Outline each blood parasite and name the species.
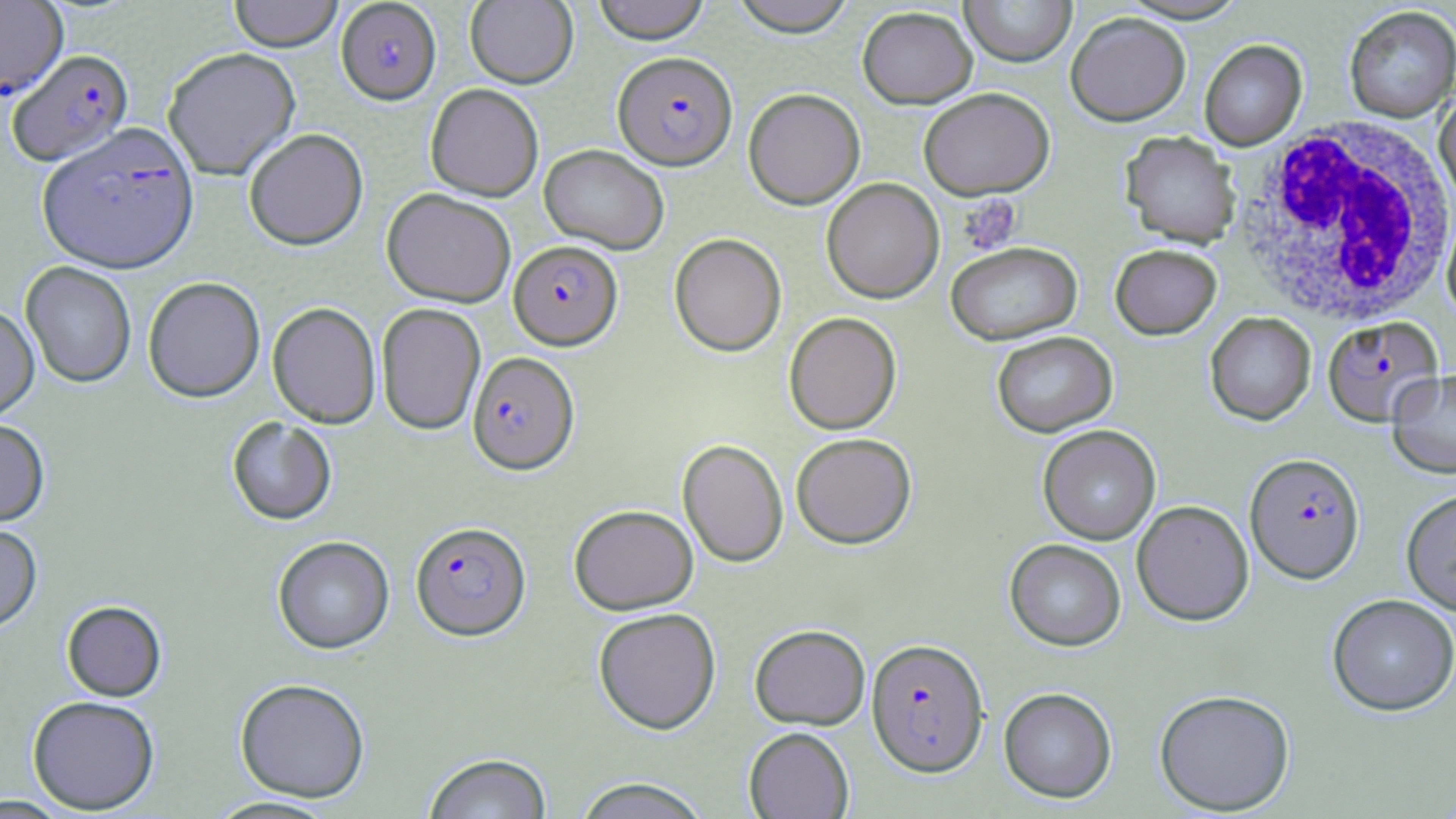

Approximate bounding boxes as named x1/y1/x2/y2 corners in pixels.
Plasmodium falciparum-infected red blood cells: (x1=0, y1=0, x2=67, y2=102), (x1=335, y1=1, x2=442, y2=106), (x1=7, y1=50, x2=134, y2=168), (x1=614, y1=51, x2=737, y2=169), (x1=37, y1=128, x2=199, y2=277), (x1=508, y1=241, x2=622, y2=350), (x1=1322, y1=315, x2=1443, y2=425), (x1=467, y1=352, x2=579, y2=476), (x1=1245, y1=452, x2=1364, y2=583), (x1=410, y1=521, x2=531, y2=642), (x1=866, y1=638, x2=988, y2=777).
No Plasmodium ovale, Plasmodium malariae, Plasmodium vivax, Babesia divergens, or Trypanosoma brucei observed.

Platelet locations: (x1=958, y1=194, x2=1022, y2=255). White blood cell locations: (x1=1233, y1=117, x2=1455, y2=326). Uninfected red blood cell locations: (x1=228, y1=0, x2=343, y2=54), (x1=465, y1=0, x2=578, y2=88), (x1=592, y1=0, x2=711, y2=43), (x1=729, y1=0, x2=857, y2=36), (x1=959, y1=0, x2=1076, y2=66), (x1=857, y1=5, x2=977, y2=109), (x1=1344, y1=5, x2=1456, y2=123), (x1=1066, y1=11, x2=1191, y2=126), (x1=1199, y1=39, x2=1307, y2=150), (x1=162, y1=49, x2=301, y2=180), (x1=425, y1=84, x2=544, y2=201), (x1=919, y1=87, x2=1054, y2=199), (x1=743, y1=88, x2=865, y2=209), (x1=1434, y1=91, x2=1456, y2=209), (x1=244, y1=129, x2=368, y2=252), (x1=1120, y1=131, x2=1242, y2=248), (x1=539, y1=143, x2=669, y2=254), (x1=821, y1=178, x2=945, y2=303), (x1=381, y1=189, x2=516, y2=308), (x1=1440, y1=202, x2=1456, y2=323), (x1=669, y1=233, x2=786, y2=356), (x1=945, y1=241, x2=1083, y2=345), (x1=1110, y1=244, x2=1222, y2=339), (x1=21, y1=262, x2=136, y2=390), (x1=143, y1=278, x2=265, y2=404), (x1=267, y1=303, x2=381, y2=428), (x1=376, y1=304, x2=485, y2=435), (x1=0, y1=305, x2=39, y2=424), (x1=784, y1=312, x2=901, y2=434), (x1=1205, y1=312, x2=1315, y2=425), (x1=992, y1=331, x2=1117, y2=437), (x1=1387, y1=369, x2=1456, y2=479), (x1=227, y1=417, x2=337, y2=526), (x1=0, y1=421, x2=50, y2=528), (x1=1037, y1=425, x2=1161, y2=544), (x1=791, y1=432, x2=917, y2=549), (x1=677, y1=439, x2=788, y2=567), (x1=1401, y1=488, x2=1456, y2=615), (x1=1132, y1=500, x2=1254, y2=625), (x1=569, y1=504, x2=698, y2=615), (x1=0, y1=525, x2=42, y2=636), (x1=272, y1=537, x2=394, y2=655), (x1=1005, y1=539, x2=1126, y2=651), (x1=1328, y1=593, x2=1456, y2=715), (x1=61, y1=601, x2=167, y2=702), (x1=593, y1=607, x2=721, y2=735), (x1=750, y1=624, x2=870, y2=729), (x1=234, y1=679, x2=370, y2=803), (x1=999, y1=687, x2=1117, y2=803), (x1=1154, y1=688, x2=1296, y2=815), (x1=27, y1=697, x2=160, y2=814), (x1=744, y1=727, x2=854, y2=818), (x1=423, y1=752, x2=553, y2=819), (x1=572, y1=777, x2=711, y2=819), (x1=0, y1=794, x2=74, y2=818), (x1=203, y1=796, x2=343, y2=818). Slide-level diagnosis: Plasmodium falciparum. Light microscopy. Captured at 1000x magnification. Image is 1456×819 pixels. Thin blood film. Single field of view. May-Grünwald-Giemsa-stained preparation.